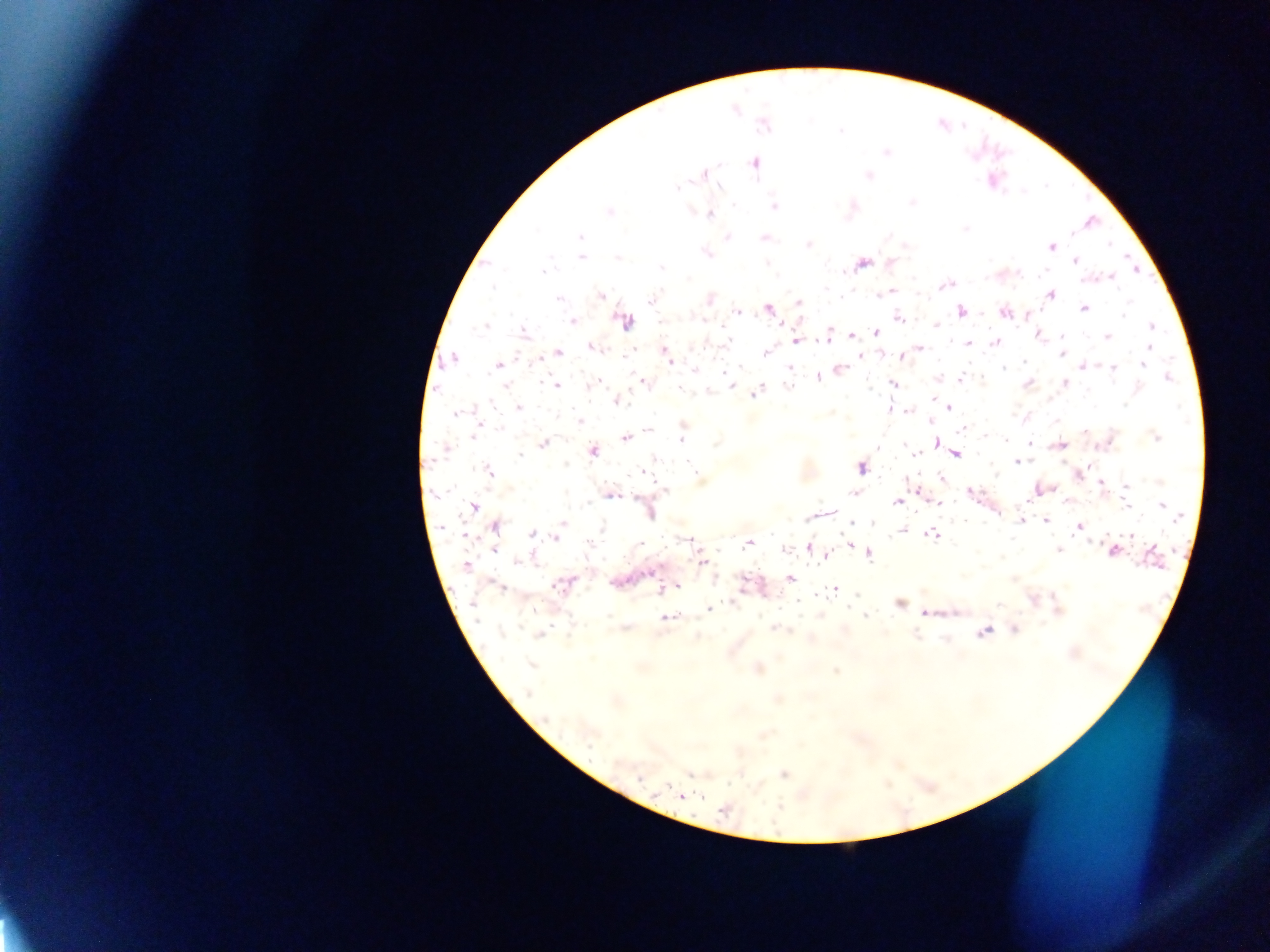

Approximate centers as (x, y) in pixels. Plasmodium parasite locations: (764, 125), (840, 130), (887, 151), (754, 163), (704, 175), (868, 176), (676, 188), (912, 204), (734, 205), (774, 206), (609, 211), (710, 214), (966, 228), (580, 237), (727, 237), (764, 238), (1110, 244), (808, 245), (1051, 247), (707, 254), (581, 257), (617, 258), (1074, 260), (863, 262), (767, 263), (891, 263), (661, 268), (543, 270), (1111, 278), (945, 285), (493, 288), (827, 289), (891, 292), (1050, 294), (601, 295), (709, 299), (558, 300), (651, 300), (800, 303), (1084, 309), (768, 310), (961, 310), (737, 311), (1125, 311), (1004, 313), (899, 318), (702, 319), (572, 321), (625, 322), (936, 325), (485, 326), (1151, 326), (524, 332), (876, 332), (828, 334), (1038, 334), (852, 335), (1107, 336), (1062, 337), (728, 341), (796, 341), (969, 342), (996, 342), (1149, 347), (594, 348), (918, 349), (559, 352), (766, 352), (1061, 353), (666, 355), (861, 356), (901, 356), (453, 359), (669, 359), (538, 360), (1024, 362), (1143, 364), (498, 365), (1083, 365), (740, 368), (790, 368), (1004, 368), (1113, 368), (841, 369), (695, 370), (1168, 377), (819, 378), (960, 380), (642, 382), (1065, 382), (595, 383), (893, 383), (1029, 383), (505, 386), (556, 386), (731, 386), (788, 386), (681, 389), (755, 394), (934, 398), (617, 401), (1125, 404), (519, 407), (948, 408), (890, 409), (908, 411), (455, 413), (580, 422), (931, 422), (962, 429), (649, 430), (1085, 432), (474, 436), (1156, 437), (625, 438), (680, 440), (1005, 440), (936, 443), (1030, 443), (544, 444), (1060, 445), (446, 449), (592, 452), (956, 454), (519, 455), (915, 455), (1018, 462), (689, 463), (861, 468), (488, 471), (645, 472), (941, 478), (1101, 483), (1126, 486), (664, 490), (969, 491), (853, 493), (610, 494), (897, 502), (938, 503), (1124, 504), (474, 506), (1163, 506), (649, 511), (1177, 517), (1141, 518), (1020, 521), (1047, 521), (563, 524), (851, 525), (496, 527), (1080, 527), (902, 531), (1131, 533), (532, 534), (932, 535), (557, 537), (688, 540), (848, 542), (748, 543), (640, 544), (810, 547), (494, 549), (786, 549), (1059, 550), (1113, 551), (869, 554), (827, 555), (518, 561), (701, 561), (467, 564), (790, 578), (499, 586), (563, 586), (675, 586), (833, 589), (899, 604), (999, 605), (709, 609), (535, 610), (925, 613), (665, 617), (866, 617), (775, 628), (1014, 629), (983, 632), (538, 636), (532, 666), (759, 669), (836, 671), (529, 693), (547, 718), (589, 743), (784, 775), (639, 778), (681, 797), (723, 811). Thick blood film. Sample from Ghana. Photographed through a microscope with a mobile-phone camera. Single field of view. Image is 1270×952 pixels.